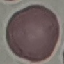

Summary:
  - Result: negative for malaria parasites
  - Capture: smartphone camera at the microscope eyepiece
  - Image type: automatically extracted cell patch, resized to 64 × 64 pixels
  - Stain: Giemsa
  - Preparation: thin smear